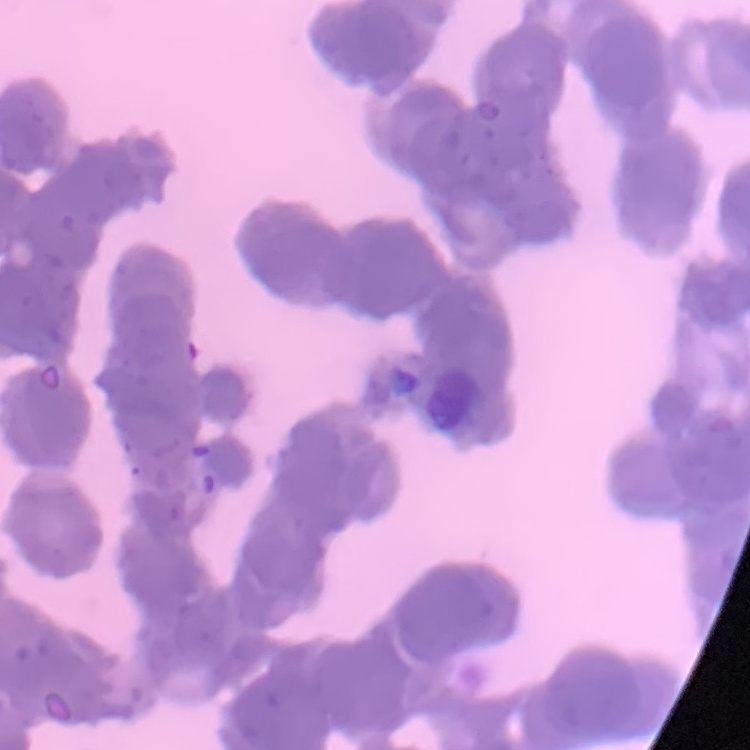

{
  "red_blood_cell_morphology": "rouleaux formation",
  "stain": "Field's or Giemsa",
  "image_type": "square crop of a larger photomicrograph",
  "preparation": "thin blood film"
}